Comment on the morphology of the red blood cells.
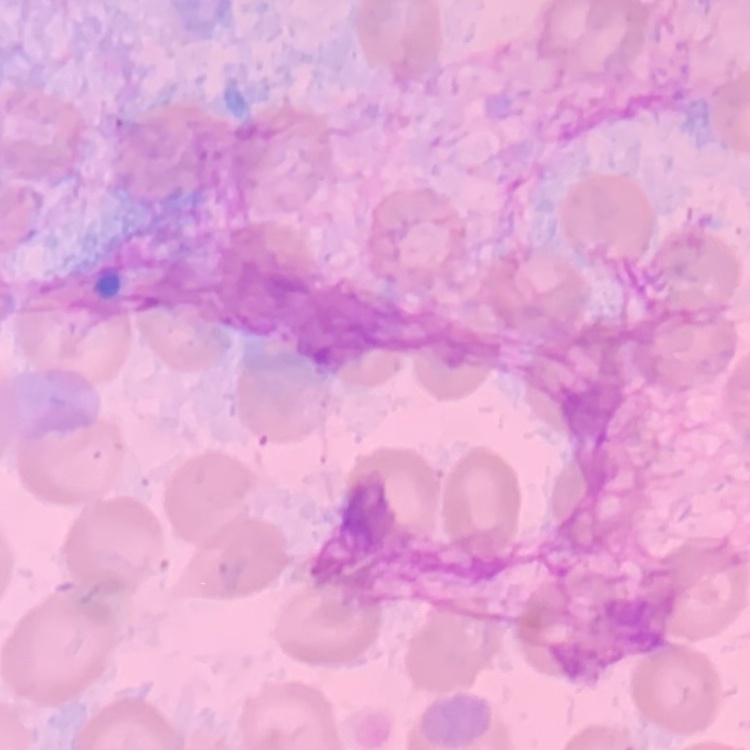
They show no rouleaux formation.

Summary:
  - Stain: Field's or Giemsa
  - Preparation: thin peripheral smear
  - Image type: one tile cut from a larger photomicrograph